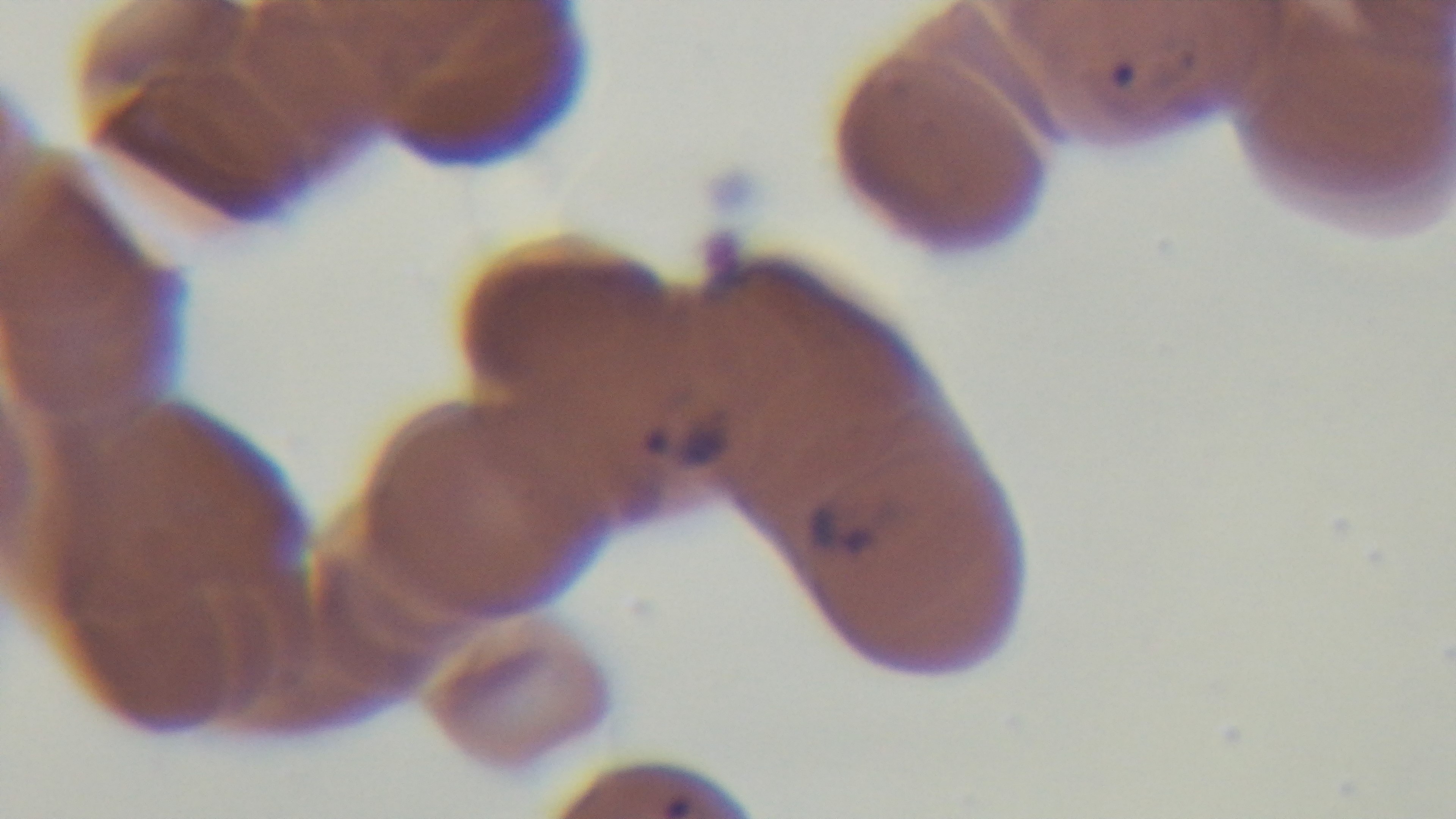
Summary:
  - Modality: light microscopy
  - Stain: Giemsa
  - Preparation: thin blood film
  - Malaria status: positive
  - Objective: 100x oil immersion
  - Capture: mounted 4K digital camera
  - Field of view: one from the slide